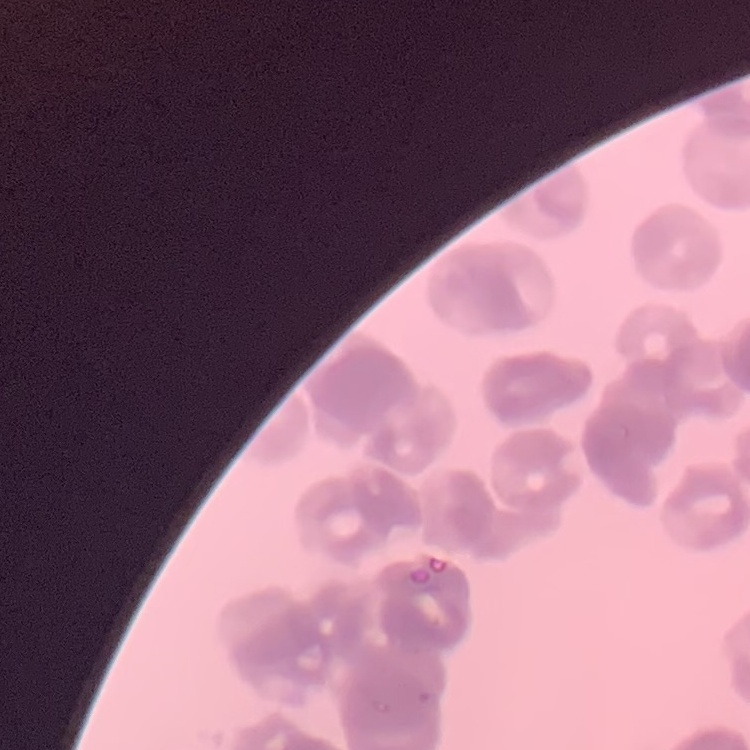

The erythrocytes show rouleaux formation. Thin blood smear. Square crop of a larger photomicrograph. Field's or Giemsa stain.